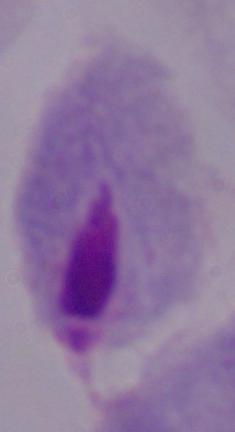

identification = trichomonad
modality = micrograph
magnification = 1000x